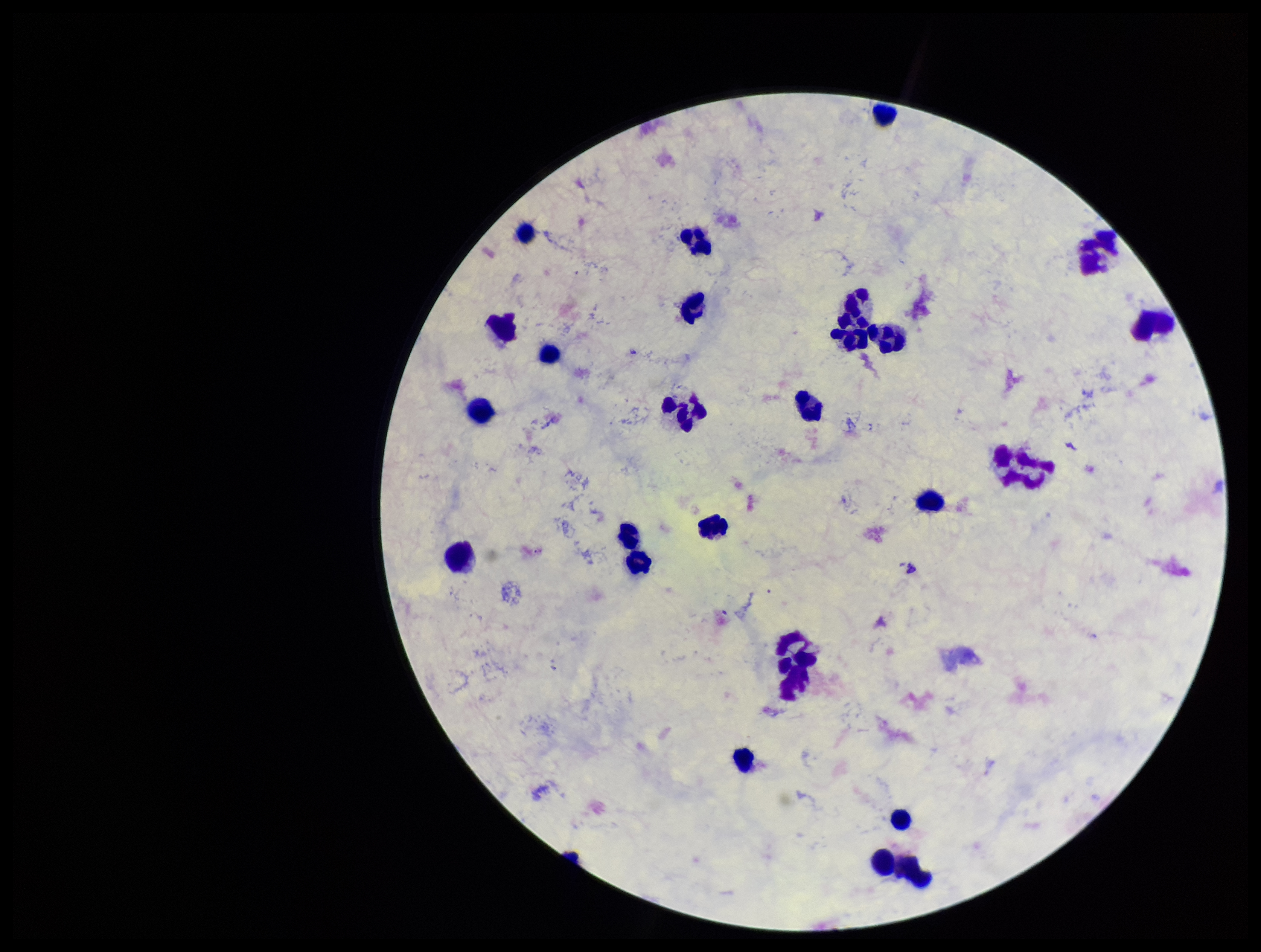 Preparation: thick blood smear. Giemsa stain. One field from this slide. Leukocyte count: 26. Image is 1261×952 pixels. Plasmodium parasites: none detected. Smartphone photograph taken through the eyepiece of a microscope. Parasite count: 0. Patient malaria status: negative.